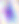
400x magnification. Photomicrograph. Toxoplasma gondii is seen.